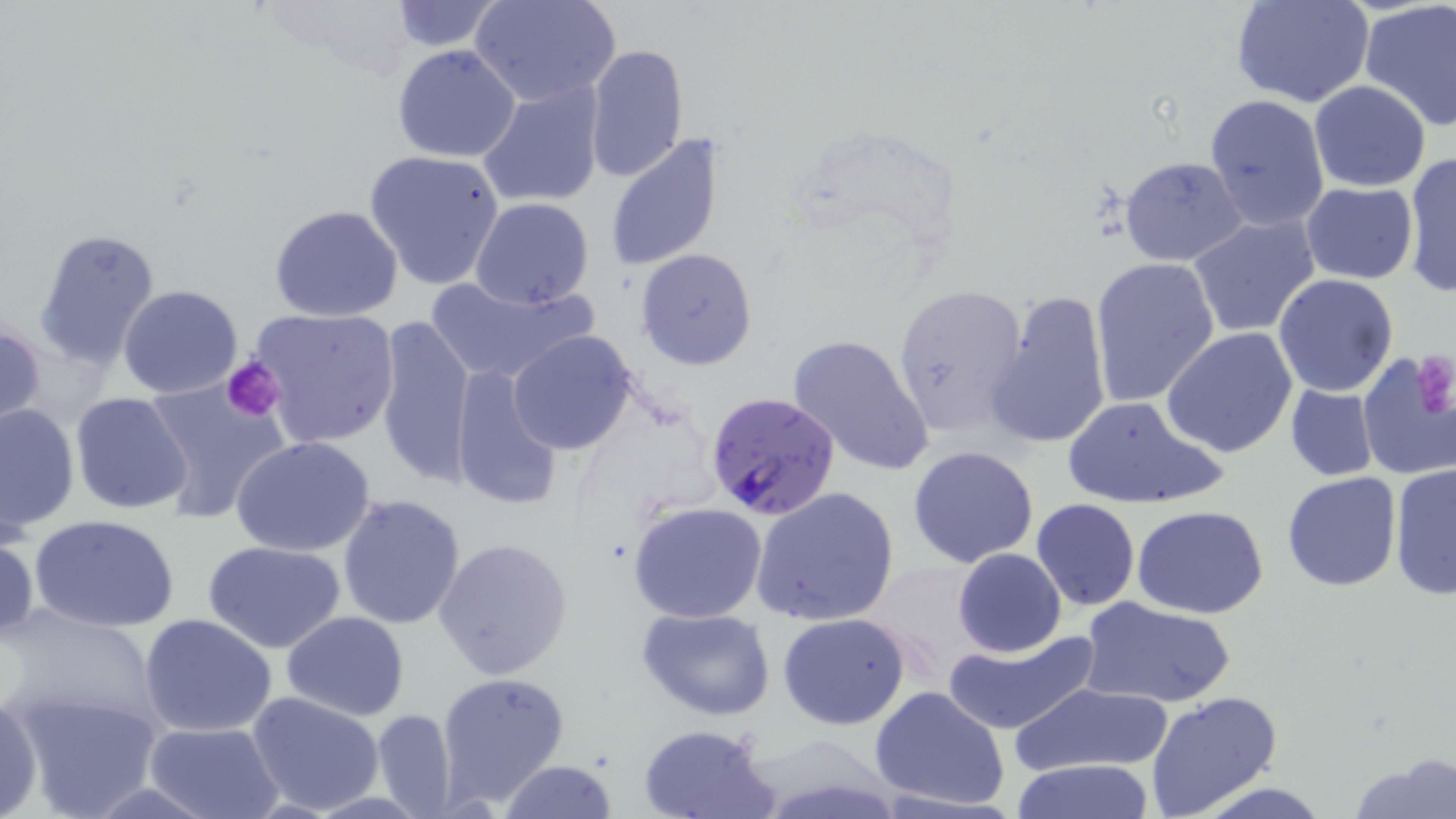 Approximate bounding boxes as named x1/y1/x2/y2 corners in pixels. Plasmodium falciparum-infected red blood cell locations: (x1=706, y1=392, x2=841, y2=520). Platelet locations: (x1=1410, y1=349, x2=1456, y2=420), (x1=225, y1=355, x2=284, y2=424). Uninfected red blood cell locations: (x1=387, y1=0, x2=507, y2=52), (x1=470, y1=0, x2=621, y2=106), (x1=1230, y1=0, x2=1374, y2=107), (x1=1361, y1=1, x2=1456, y2=131), (x1=584, y1=43, x2=689, y2=185), (x1=391, y1=44, x2=521, y2=163), (x1=477, y1=79, x2=605, y2=208), (x1=1308, y1=81, x2=1430, y2=192), (x1=1203, y1=93, x2=1329, y2=231), (x1=605, y1=134, x2=726, y2=271), (x1=364, y1=150, x2=506, y2=292), (x1=1402, y1=151, x2=1456, y2=298), (x1=1118, y1=155, x2=1248, y2=266), (x1=1300, y1=182, x2=1417, y2=284), (x1=469, y1=198, x2=594, y2=308), (x1=267, y1=204, x2=405, y2=323), (x1=1188, y1=214, x2=1322, y2=339), (x1=34, y1=228, x2=162, y2=370), (x1=635, y1=248, x2=758, y2=371), (x1=1090, y1=256, x2=1220, y2=408), (x1=423, y1=272, x2=597, y2=386), (x1=1273, y1=272, x2=1400, y2=396), (x1=890, y1=281, x2=1029, y2=439), (x1=117, y1=284, x2=244, y2=399), (x1=985, y1=286, x2=1111, y2=451), (x1=247, y1=307, x2=401, y2=449), (x1=374, y1=315, x2=475, y2=491), (x1=0, y1=320, x2=45, y2=435), (x1=1161, y1=329, x2=1299, y2=460), (x1=507, y1=331, x2=640, y2=456), (x1=788, y1=333, x2=936, y2=477), (x1=1355, y1=350, x2=1456, y2=482), (x1=448, y1=366, x2=563, y2=513), (x1=140, y1=376, x2=292, y2=525), (x1=1284, y1=384, x2=1379, y2=482), (x1=70, y1=392, x2=194, y2=514), (x1=1061, y1=396, x2=1222, y2=510), (x1=0, y1=400, x2=80, y2=535), (x1=231, y1=435, x2=377, y2=557), (x1=907, y1=445, x2=1040, y2=567), (x1=1390, y1=462, x2=1456, y2=601), (x1=1282, y1=472, x2=1401, y2=591), (x1=750, y1=486, x2=901, y2=628), (x1=336, y1=493, x2=467, y2=631), (x1=1031, y1=499, x2=1140, y2=611), (x1=627, y1=500, x2=770, y2=623), (x1=1133, y1=505, x2=1271, y2=618), (x1=29, y1=514, x2=181, y2=633), (x1=0, y1=525, x2=38, y2=644), (x1=433, y1=537, x2=573, y2=681), (x1=203, y1=540, x2=347, y2=653), (x1=952, y1=548, x2=1067, y2=657), (x1=1079, y1=597, x2=1235, y2=708), (x1=2, y1=607, x2=163, y2=731), (x1=636, y1=607, x2=775, y2=719), (x1=281, y1=610, x2=409, y2=721), (x1=777, y1=611, x2=913, y2=730), (x1=139, y1=613, x2=276, y2=737), (x1=942, y1=628, x2=1100, y2=736), (x1=435, y1=670, x2=571, y2=808), (x1=1007, y1=681, x2=1172, y2=779), (x1=7, y1=684, x2=164, y2=817), (x1=868, y1=686, x2=1012, y2=812), (x1=0, y1=692, x2=43, y2=819), (x1=247, y1=692, x2=383, y2=815), (x1=1144, y1=692, x2=1282, y2=817), (x1=373, y1=709, x2=461, y2=813), (x1=141, y1=721, x2=285, y2=819), (x1=637, y1=724, x2=779, y2=819), (x1=1352, y1=756, x2=1456, y2=819), (x1=497, y1=759, x2=619, y2=818), (x1=1007, y1=759, x2=1159, y2=817). Slide-level diagnosis: Plasmodium falciparum. Light microscopy. May-Grünwald-Giemsa stain. Image is 1456×819 pixels. Single field of view. Thin blood smear. 1000x magnification.